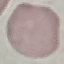

malaria status = uninfected
stain = Giemsa
preparation = thin blood film
capture = smartphone camera at the microscope eyepiece
image type = cell patch, automatically extracted from a larger field of view and resized to 64 × 64 pixels